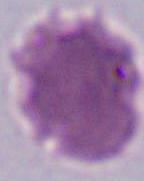 Photomicrograph. Captured at 1000x magnification. A red blood cell is seen.